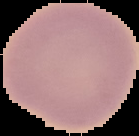

preparation = thin blood smear
malaria status = uninfected
image size = 139×136 pixels
image type = cell region segmented out of the field of view; surrounding area masked to black